Classify this cell by malaria status.
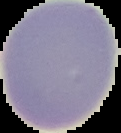
Uninfected.

image_size: 121×133 pixels
preparation: thin blood film
image_type: segmented cell region with the area outside set to black